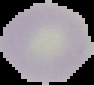
Summary:
  - Preparation: thin blood smear
  - Image size: 94×85 pixels
  - Malaria status: uninfected
  - Image type: segmented cell region on a black background